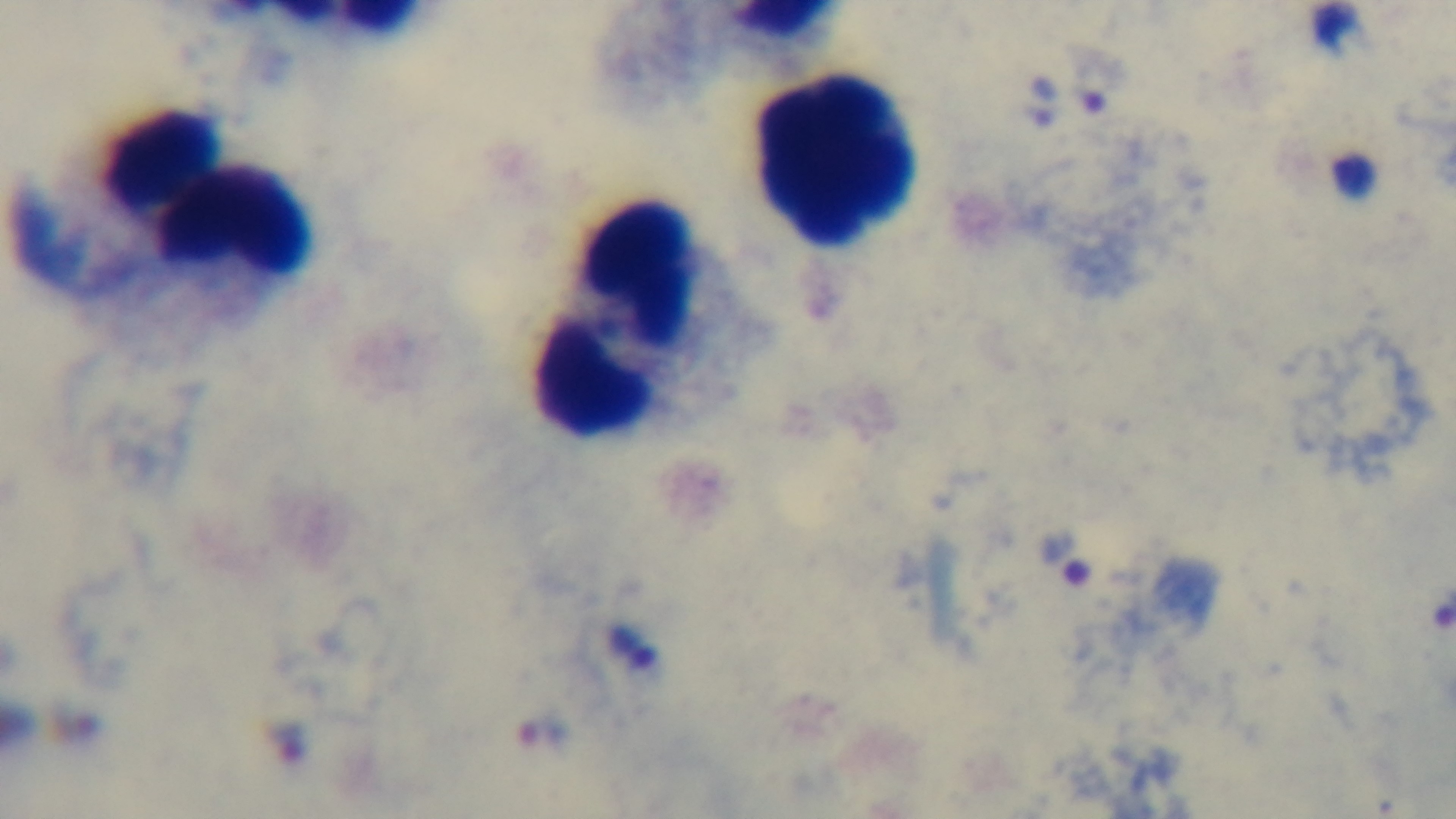
modality = light microscopy
capture = mounted 4K digital camera
preparation = thick
malaria status = positive
stain = Giemsa
objective = 100x oil immersion
field of view = one from the slide